Classify this cell by malaria status.
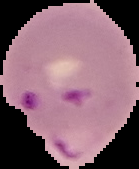

Parasitized.

Cell region segmented out of the field of view; the surrounding area is masked to black. Image is 139×169 pixels. From a thin blood smear.